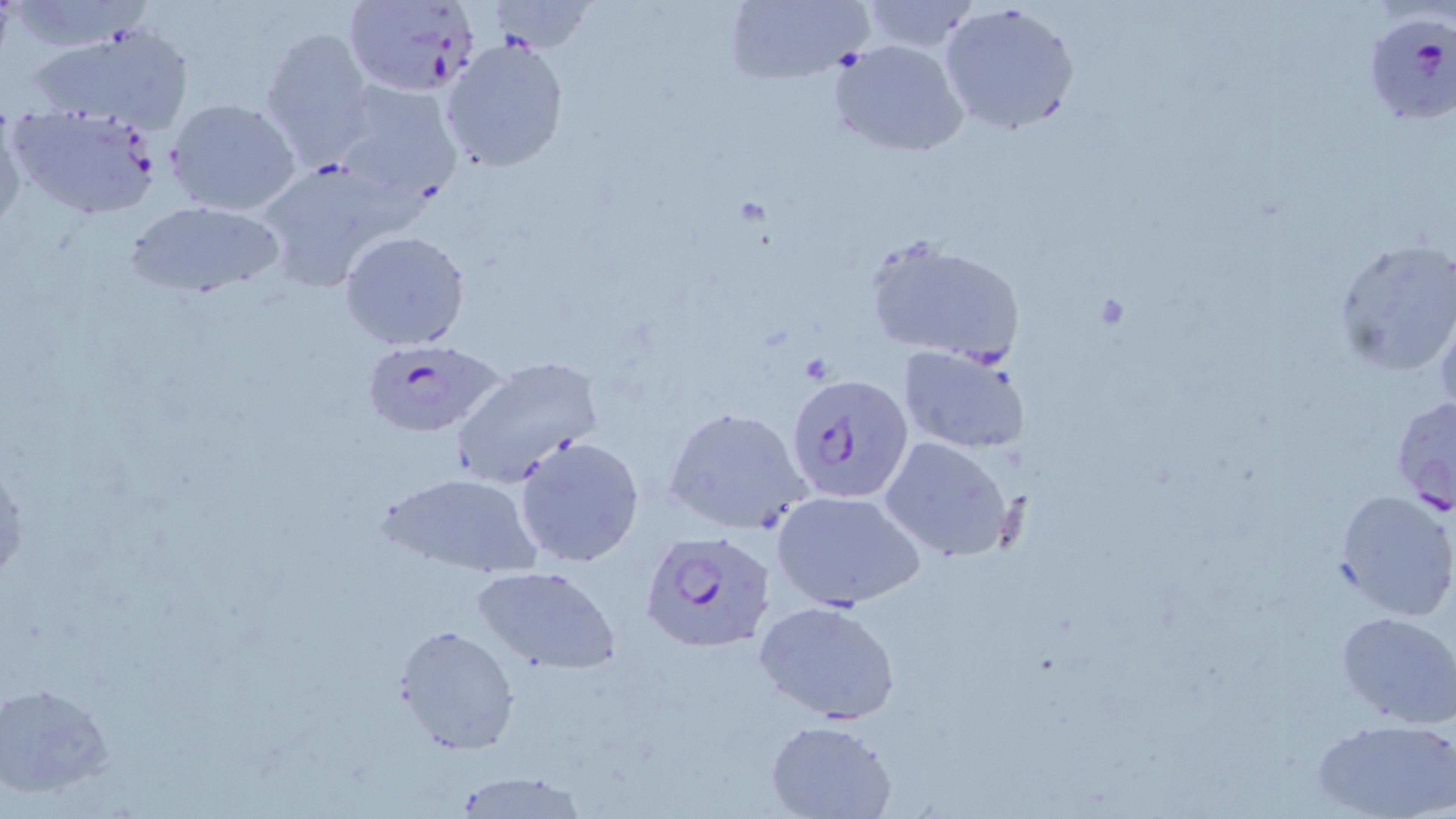

Summary:
  - Coordinate format: approximate bounding boxes as (x1,y1)-(x2,y2) corner pairs in pixels
  - Uninfected red blood cell locations: (722,0)-(873,87), (854,0)-(984,54), (938,2)-(1080,138), (24,22)-(195,134), (258,27)-(374,166), (442,30)-(573,170), (829,40)-(968,158), (329,80)-(466,207), (165,97)-(302,216), (0,103)-(29,237), (251,157)-(421,293), (124,199)-(286,299), (340,230)-(472,352), (865,236)-(1025,366), (1331,239)-(1456,379), (1433,288)-(1456,419), (899,344)-(1031,455), (450,356)-(603,486), (663,406)-(814,535), (514,435)-(646,569), (880,437)-(1014,563), (376,472)-(543,582), (771,488)-(927,611), (1333,488)-(1455,621), (471,565)-(623,676), (754,599)-(903,725), (1335,611)-(1456,729), (393,623)-(522,755), (0,682)-(116,797), (1311,717)-(1454,819), (763,719)-(897,819), (446,773)-(589,819)
  - Plasmodium falciparum-infected red blood cell locations: (341,1)-(482,98), (1362,10)-(1455,124), (10,103)-(164,221), (356,338)-(507,438), (787,376)-(912,503), (1389,393)-(1456,514), (639,530)-(777,652)
  - Slide-level diagnosis: Plasmodium falciparum
  - Magnification: 1000x
  - Modality: optical microscopy
  - Field of view: single
  - Stain: May-Grünwald-Giemsa
  - Preparation: thin blood film
  - Image size: 1456×819 pixels